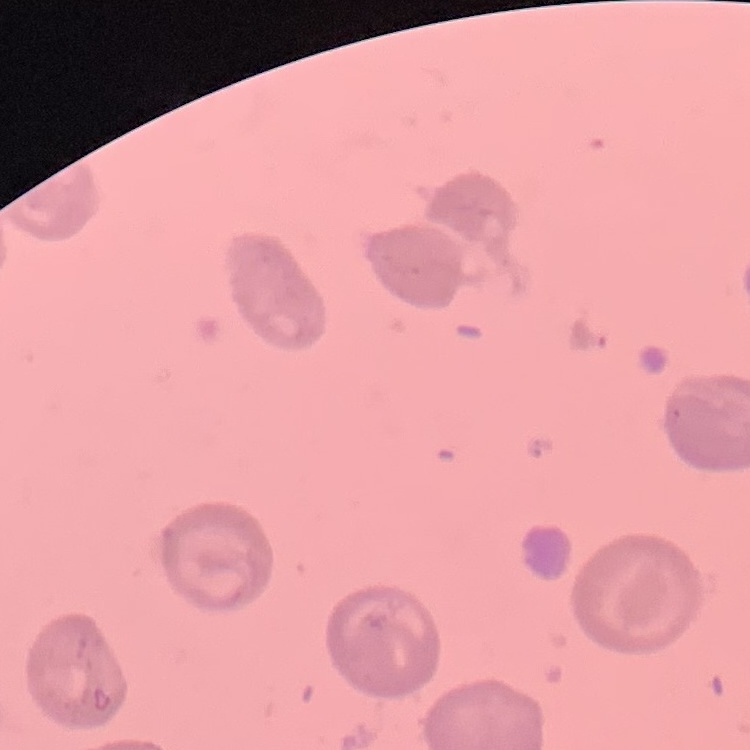
red blood cell morphology = no rouleaux formation
preparation = thin peripheral smear
image type = one tile cut from a larger photomicrograph
stain = Field's or Giemsa